Find the cells and give the type of each one.
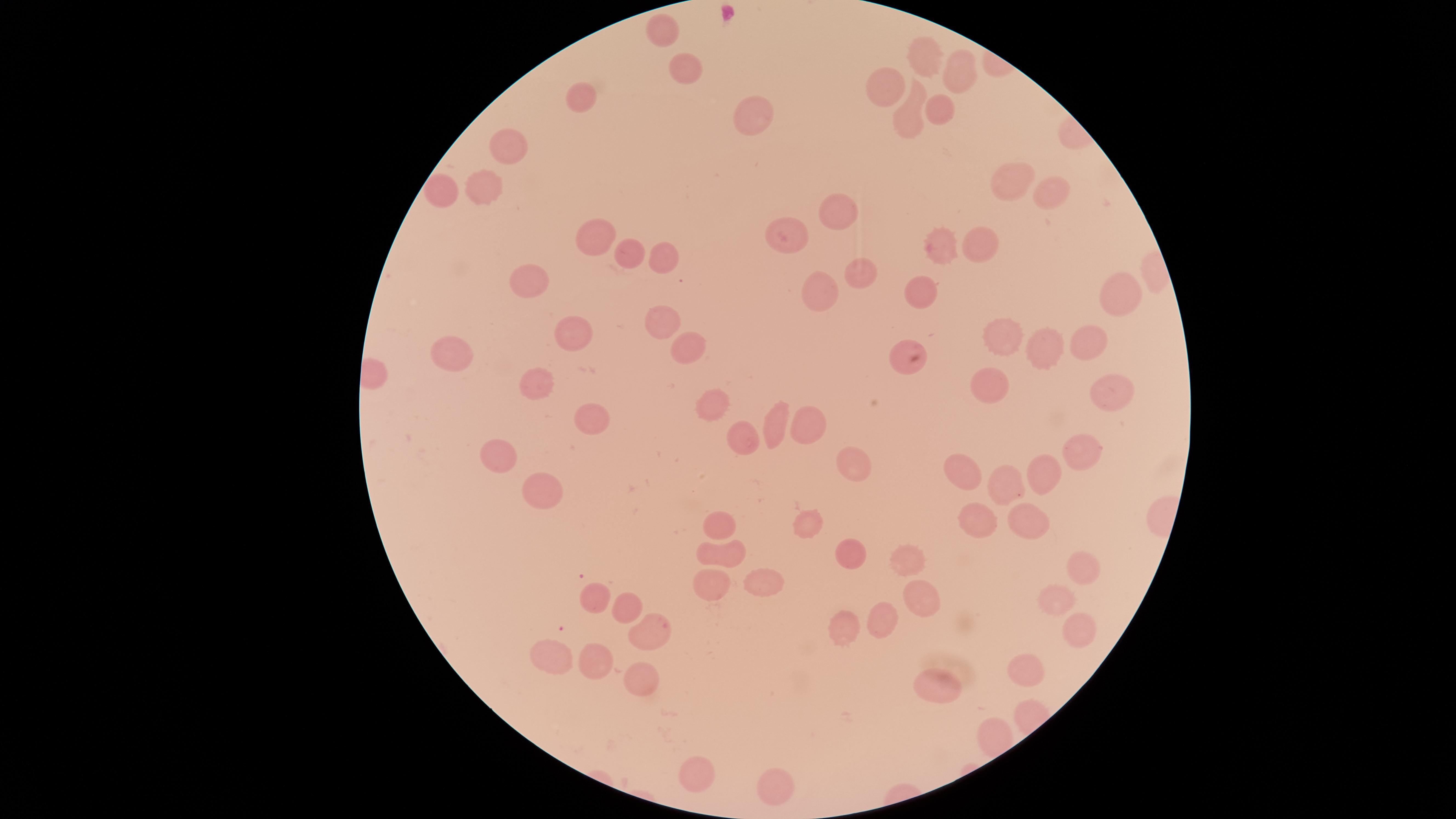
No parasitized red blood cells identified.
Approximate marker points as (x, y) in pixels.
Uninfected red blood cells: (666, 30), (924, 59), (960, 72), (687, 73), (883, 88), (582, 94), (938, 108), (748, 113), (912, 118), (510, 144), (1006, 178), (1044, 189), (484, 191), (449, 194), (836, 213), (602, 231), (793, 232), (979, 241), (940, 245), (630, 251), (668, 260), (857, 273), (527, 279), (817, 289), (921, 291), (1117, 292), (663, 328), (1090, 334), (1005, 335), (575, 337), (686, 344), (1049, 348), (455, 356), (903, 362), (540, 385), (989, 385), (1111, 388), (710, 402), (584, 418), (804, 427), (771, 429), (742, 443), (1084, 451), (500, 461), (971, 466), (852, 467), (1043, 472), (1012, 484), (540, 491), (974, 521), (718, 522), (1026, 522), (809, 526), (722, 553), (855, 554), (912, 559), (1083, 566), (759, 577), (710, 583), (590, 597), (921, 598), (1052, 599), (626, 607), (882, 617), (848, 631), (649, 634), (1089, 639), (559, 654), (597, 662), (1028, 665), (637, 676), (938, 686), (695, 777), (774, 786).
No white blood cells identified.

One field of view of the specimen. Photographed with a smartphone camera through the microscope eyepiece. Image is 1456×819 pixels. Thin blood smear. The visible region is circular. Giemsa stain.